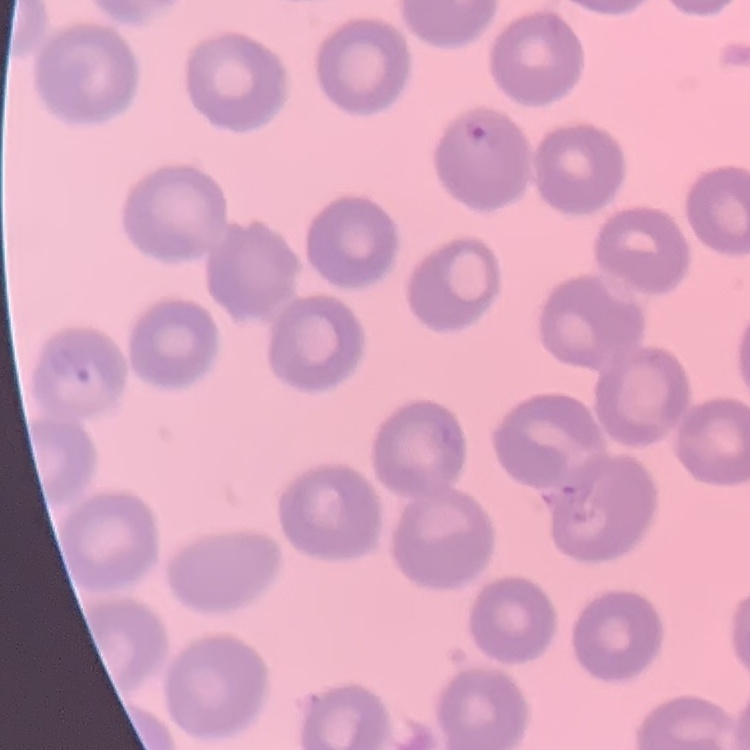
Summary:
  - Erythrocyte morphology: no rouleaux formation
  - Preparation: thin blood smear
  - Stain: Field's or Giemsa
  - Image type: square crop of a larger photomicrograph